Assess this cell for malaria.
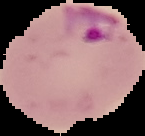

It is parasitized.

preparation: thin blood film
image_size: 145×136 pixels
image_type: segmented cell region with the area outside set to black